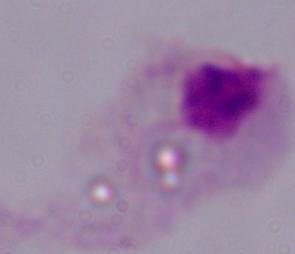
Summary:
  - Modality: photomicrograph
  - Magnification: 1000x
  - Identification: trichomonad